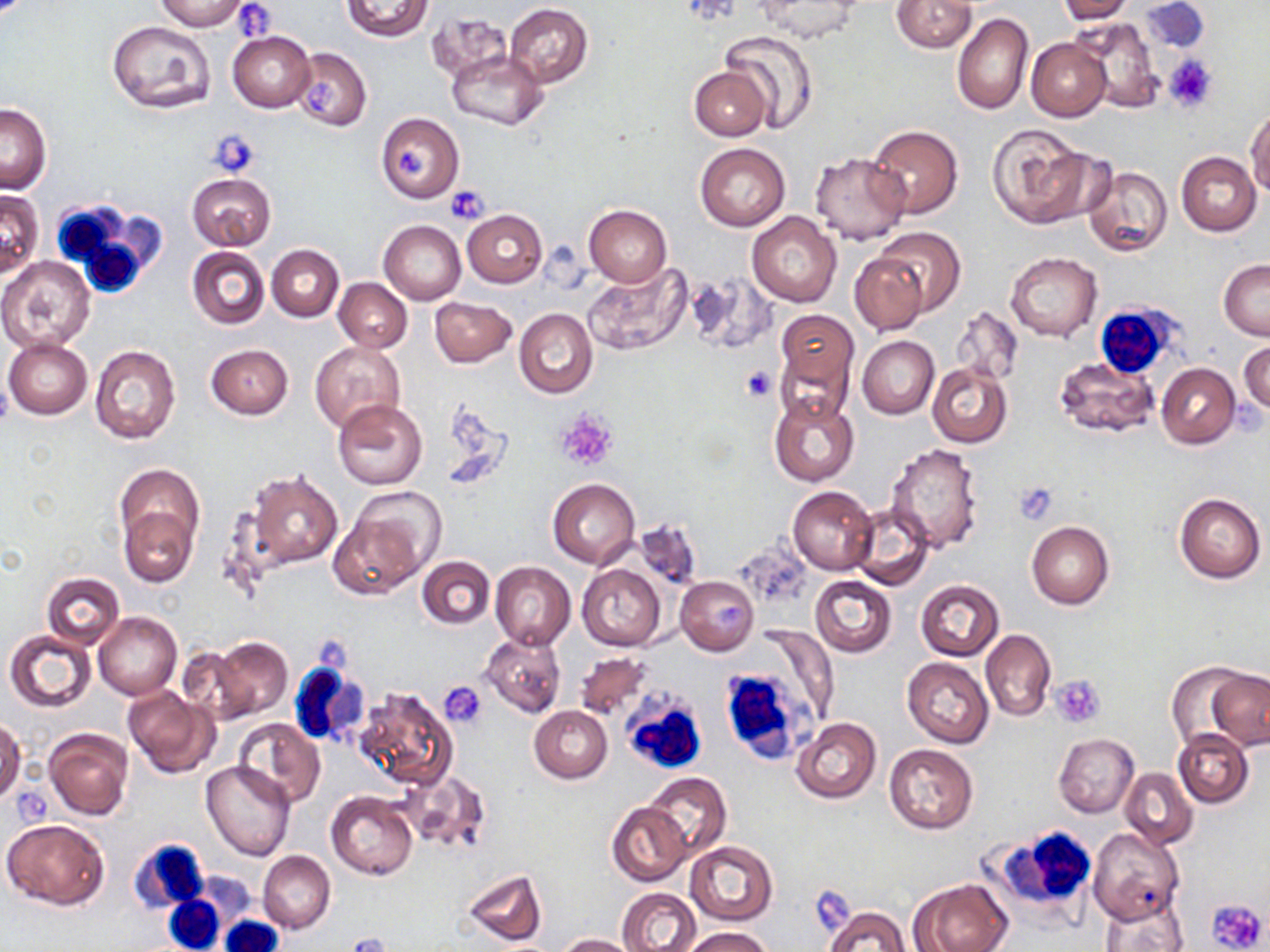
Summary:
  - Coordinate format: approximate bounding boxes as named x1/y1/x2/y2 corners in pixels
  - Platelet locations: (x1=232, y1=3, x2=275, y2=37), (x1=1163, y1=56, x2=1217, y2=112), (x1=307, y1=78, x2=339, y2=111), (x1=207, y1=130, x2=260, y2=179), (x1=395, y1=145, x2=426, y2=177), (x1=444, y1=185, x2=489, y2=224), (x1=739, y1=364, x2=778, y2=401), (x1=556, y1=410, x2=617, y2=469), (x1=1014, y1=482, x2=1058, y2=524), (x1=1051, y1=675, x2=1105, y2=727), (x1=440, y1=682, x2=487, y2=729), (x1=1207, y1=897, x2=1269, y2=950), (x1=343, y1=931, x2=391, y2=952)
  - White blood cell locations: (x1=49, y1=199, x2=166, y2=301), (x1=1097, y1=304, x2=1188, y2=384), (x1=718, y1=645, x2=826, y2=761), (x1=288, y1=658, x2=369, y2=747), (x1=621, y1=695, x2=709, y2=777), (x1=983, y1=824, x2=1098, y2=921), (x1=128, y1=839, x2=208, y2=915), (x1=163, y1=895, x2=225, y2=952), (x1=217, y1=916, x2=283, y2=952)
  - Uninfected red blood cell locations: (x1=155, y1=0, x2=249, y2=31), (x1=342, y1=0, x2=432, y2=41), (x1=892, y1=0, x2=977, y2=53), (x1=1058, y1=0, x2=1137, y2=22), (x1=755, y1=1, x2=858, y2=42), (x1=1141, y1=1, x2=1210, y2=54), (x1=504, y1=3, x2=593, y2=88), (x1=426, y1=12, x2=514, y2=83), (x1=952, y1=13, x2=1033, y2=116), (x1=1072, y1=16, x2=1163, y2=112), (x1=106, y1=19, x2=217, y2=114), (x1=718, y1=29, x2=819, y2=134), (x1=228, y1=31, x2=316, y2=112), (x1=1027, y1=38, x2=1111, y2=121), (x1=292, y1=47, x2=371, y2=131), (x1=448, y1=50, x2=548, y2=130), (x1=689, y1=66, x2=771, y2=141), (x1=1, y1=104, x2=52, y2=193), (x1=1246, y1=106, x2=1270, y2=197), (x1=376, y1=113, x2=464, y2=203), (x1=987, y1=123, x2=1096, y2=228), (x1=867, y1=125, x2=963, y2=218), (x1=694, y1=142, x2=790, y2=231), (x1=810, y1=152, x2=910, y2=246), (x1=1176, y1=152, x2=1261, y2=235), (x1=1084, y1=166, x2=1173, y2=258), (x1=187, y1=173, x2=276, y2=250), (x1=0, y1=191, x2=42, y2=277), (x1=584, y1=205, x2=673, y2=286), (x1=461, y1=210, x2=547, y2=288), (x1=747, y1=211, x2=840, y2=306), (x1=379, y1=219, x2=466, y2=304), (x1=873, y1=226, x2=966, y2=316), (x1=266, y1=244, x2=344, y2=321), (x1=187, y1=247, x2=269, y2=330), (x1=849, y1=251, x2=927, y2=334), (x1=1005, y1=251, x2=1102, y2=342), (x1=0, y1=256, x2=94, y2=353), (x1=1219, y1=259, x2=1270, y2=339), (x1=587, y1=263, x2=693, y2=357), (x1=334, y1=278, x2=412, y2=352), (x1=430, y1=295, x2=516, y2=368), (x1=513, y1=308, x2=599, y2=399), (x1=775, y1=308, x2=858, y2=395), (x1=953, y1=308, x2=1022, y2=386), (x1=858, y1=335, x2=939, y2=418), (x1=4, y1=338, x2=93, y2=420), (x1=310, y1=341, x2=405, y2=433), (x1=1239, y1=342, x2=1269, y2=415), (x1=89, y1=344, x2=180, y2=443), (x1=206, y1=344, x2=293, y2=419), (x1=1055, y1=356, x2=1157, y2=438), (x1=927, y1=362, x2=1014, y2=448), (x1=1155, y1=363, x2=1240, y2=449), (x1=769, y1=391, x2=860, y2=487), (x1=334, y1=400, x2=427, y2=488), (x1=885, y1=444, x2=983, y2=553), (x1=115, y1=462, x2=204, y2=560), (x1=242, y1=468, x2=343, y2=573), (x1=547, y1=477, x2=640, y2=568), (x1=787, y1=485, x2=879, y2=574), (x1=350, y1=486, x2=446, y2=582), (x1=1174, y1=493, x2=1266, y2=583), (x1=852, y1=503, x2=933, y2=591), (x1=119, y1=506, x2=196, y2=587), (x1=329, y1=510, x2=424, y2=599), (x1=633, y1=518, x2=703, y2=591), (x1=1026, y1=521, x2=1115, y2=610), (x1=417, y1=556, x2=495, y2=629), (x1=490, y1=562, x2=576, y2=650), (x1=578, y1=564, x2=666, y2=651), (x1=42, y1=572, x2=125, y2=650), (x1=810, y1=575, x2=896, y2=656), (x1=676, y1=576, x2=758, y2=655), (x1=915, y1=580, x2=1005, y2=661), (x1=95, y1=612, x2=181, y2=699), (x1=752, y1=625, x2=838, y2=726), (x1=982, y1=629, x2=1056, y2=721), (x1=5, y1=630, x2=96, y2=712), (x1=480, y1=631, x2=566, y2=718), (x1=208, y1=638, x2=292, y2=720), (x1=177, y1=647, x2=257, y2=724), (x1=573, y1=650, x2=652, y2=721), (x1=903, y1=658, x2=994, y2=748), (x1=1167, y1=662, x2=1256, y2=748), (x1=1208, y1=670, x2=1269, y2=748), (x1=353, y1=686, x2=457, y2=790), (x1=123, y1=687, x2=218, y2=777), (x1=529, y1=705, x2=612, y2=783), (x1=790, y1=717, x2=881, y2=804), (x1=232, y1=718, x2=325, y2=808), (x1=0, y1=719, x2=24, y2=806), (x1=44, y1=728, x2=133, y2=820), (x1=1173, y1=728, x2=1254, y2=808), (x1=1053, y1=733, x2=1139, y2=817), (x1=883, y1=744, x2=978, y2=833), (x1=201, y1=761, x2=297, y2=862), (x1=1121, y1=768, x2=1197, y2=848), (x1=399, y1=770, x2=490, y2=855), (x1=643, y1=771, x2=730, y2=861), (x1=326, y1=790, x2=418, y2=880), (x1=607, y1=801, x2=690, y2=886), (x1=3, y1=818, x2=111, y2=910), (x1=1087, y1=828, x2=1184, y2=925), (x1=686, y1=841, x2=778, y2=925), (x1=258, y1=851, x2=335, y2=933), (x1=462, y1=869, x2=548, y2=946), (x1=913, y1=878, x2=1011, y2=952), (x1=616, y1=888, x2=702, y2=952), (x1=1100, y1=894, x2=1188, y2=951), (x1=823, y1=905, x2=911, y2=952), (x1=681, y1=927, x2=772, y2=951), (x1=557, y1=933, x2=637, y2=952)
  - Slide-level diagnosis: no evidence of blood parasites
  - Modality: optical microscopy
  - Image size: 1270×952 pixels
  - Field of view: one of a larger specimen
  - Magnification: 1000x
  - Stain: May-Grünwald-Giemsa
  - Preparation: thin blood smear